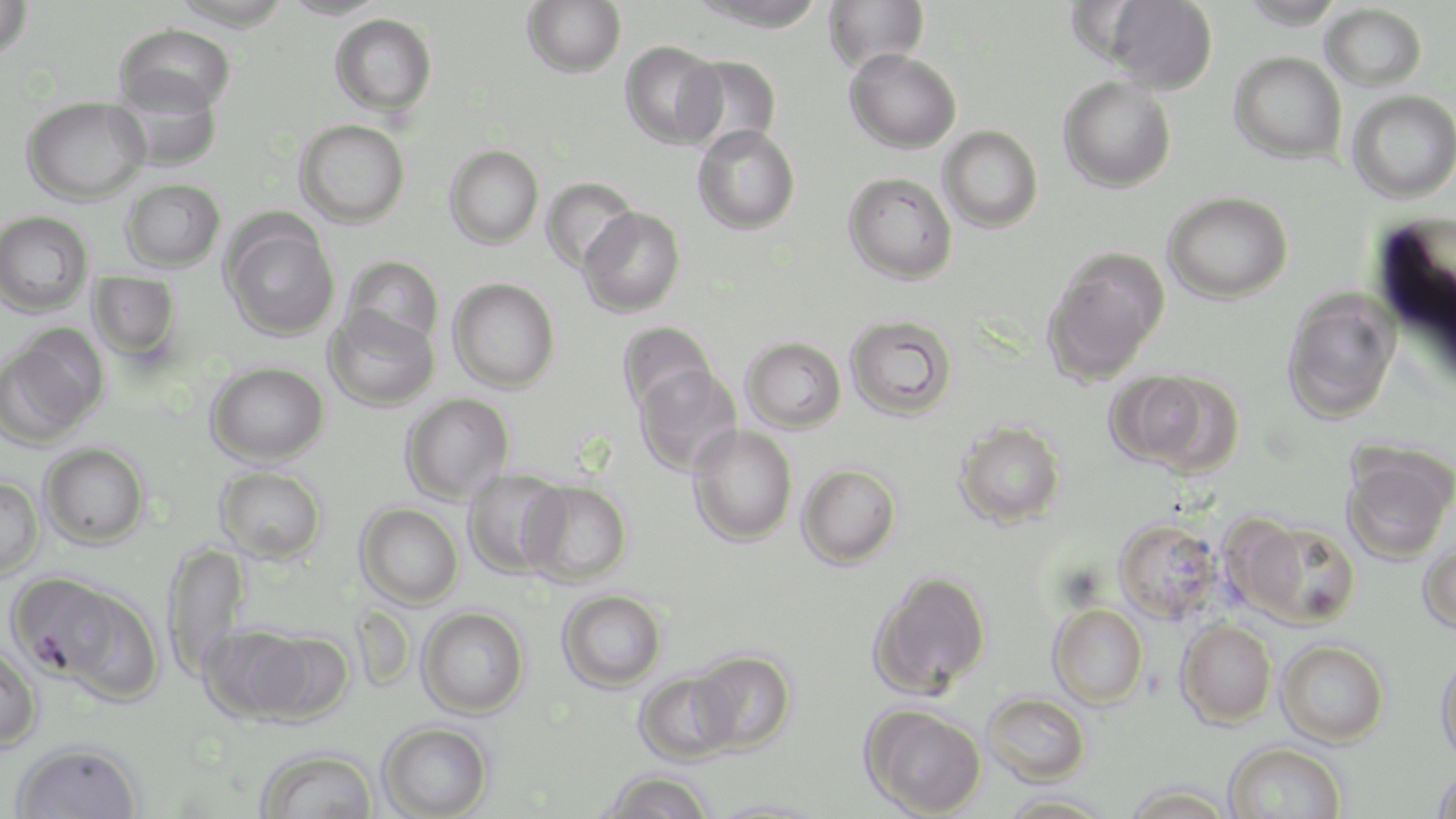

Summary:
  - Coordinate format: approximate bounding boxes as (x1, y1, x2, y2) in pixels
  - Uninfected red blood cell locations: (0, 0, 33, 60), (169, 0, 294, 30), (280, 0, 392, 19), (522, 0, 626, 77), (689, 0, 830, 32), (823, 0, 929, 75), (1104, 0, 1218, 94), (1237, 0, 1346, 29), (1321, 4, 1428, 92), (330, 13, 437, 116), (115, 23, 236, 117), (619, 41, 726, 149), (844, 48, 962, 153), (1229, 51, 1347, 163), (680, 55, 782, 153), (111, 76, 222, 171), (1058, 76, 1176, 192), (1347, 89, 1456, 203), (22, 95, 149, 204), (295, 119, 410, 227), (692, 125, 800, 234), (939, 125, 1043, 232), (445, 144, 544, 249), (843, 172, 957, 284), (541, 177, 640, 274), (122, 178, 225, 271), (1163, 191, 1293, 303), (579, 206, 685, 317), (0, 210, 93, 315), (223, 219, 340, 342), (1043, 252, 1167, 382), (343, 255, 443, 350), (88, 271, 181, 361), (448, 277, 560, 392), (1283, 290, 1400, 422), (325, 305, 439, 410), (845, 314, 956, 420), (618, 320, 719, 416), (2, 328, 107, 445), (741, 336, 846, 433), (206, 362, 329, 466), (634, 363, 742, 475), (1115, 371, 1243, 474), (401, 392, 514, 504), (954, 419, 1066, 529), (688, 424, 797, 546), (40, 443, 149, 548), (1340, 447, 1455, 562), (797, 464, 901, 568), (215, 465, 327, 563), (463, 468, 570, 578), (0, 475, 43, 579), (520, 478, 632, 585), (356, 502, 463, 608), (1239, 518, 1361, 628), (1114, 519, 1224, 624), (1418, 539, 1456, 634), (163, 541, 248, 684), (868, 569, 992, 699), (23, 578, 163, 703), (558, 589, 666, 691), (1048, 604, 1149, 708), (417, 605, 529, 718), (1176, 619, 1277, 728), (198, 623, 318, 724), (250, 629, 354, 724), (1277, 639, 1389, 746), (0, 642, 43, 753), (689, 650, 796, 754), (1435, 650, 1456, 768), (633, 670, 739, 765), (982, 692, 1091, 786), (862, 704, 987, 817), (378, 721, 494, 819), (11, 739, 143, 819), (1223, 741, 1345, 819), (255, 746, 378, 818), (1432, 767, 1456, 819), (601, 770, 714, 819), (1122, 785, 1236, 818), (1000, 793, 1116, 818), (707, 797, 827, 818)
  - Slide-level diagnosis: Plasmodium falciparum
  - Magnification: 1000x
  - Image size: 1456×819 pixels
  - Modality: optical microscopy
  - Field of view: one of a larger specimen
  - Stain: May-Grünwald-Giemsa
  - Preparation: thin blood smear